Report the malaria status of this cell.
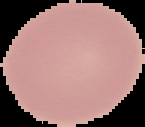

Uninfected.

image_size: 145×127 pixels
image_type: segmented cell region on a black background
preparation: thin blood film